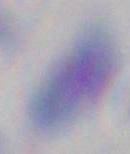
modality = micrograph
magnification = 1000x
identification = Toxoplasma gondii